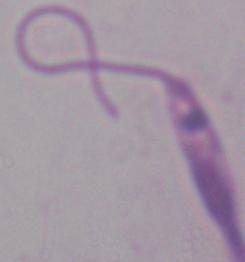
Summary:
  - Modality: micrograph
  - Magnification: 1000x
  - Identification: Leishmania